Comment on the morphology of the erythrocytes.
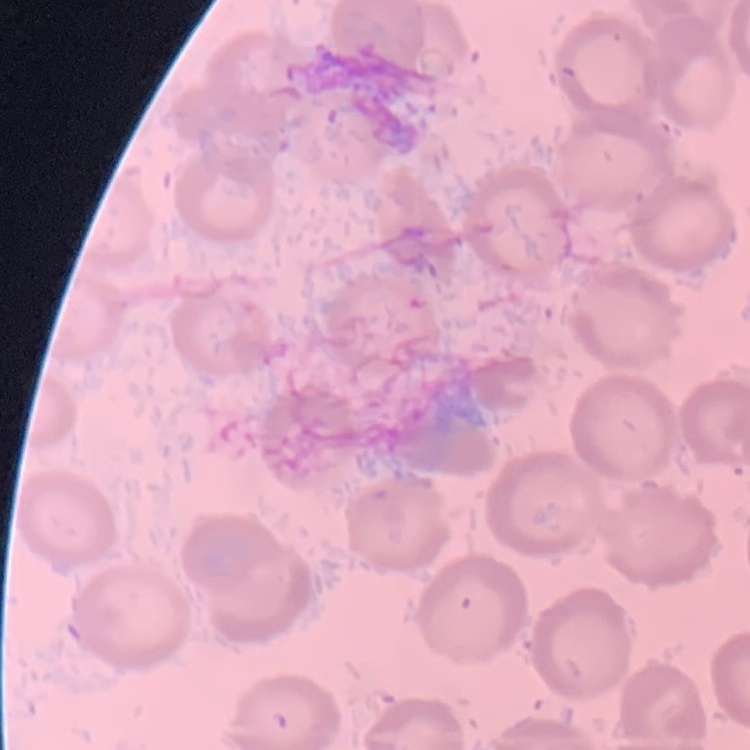

No rouleaux formation.

{
  "image_type": "one tile cut from a larger photomicrograph",
  "stain": "Field's or Giemsa",
  "preparation": "thin blood film"
}